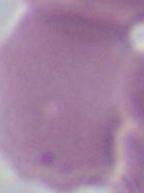
Micrograph. Captured at 1000x magnification. A red blood cell is seen.